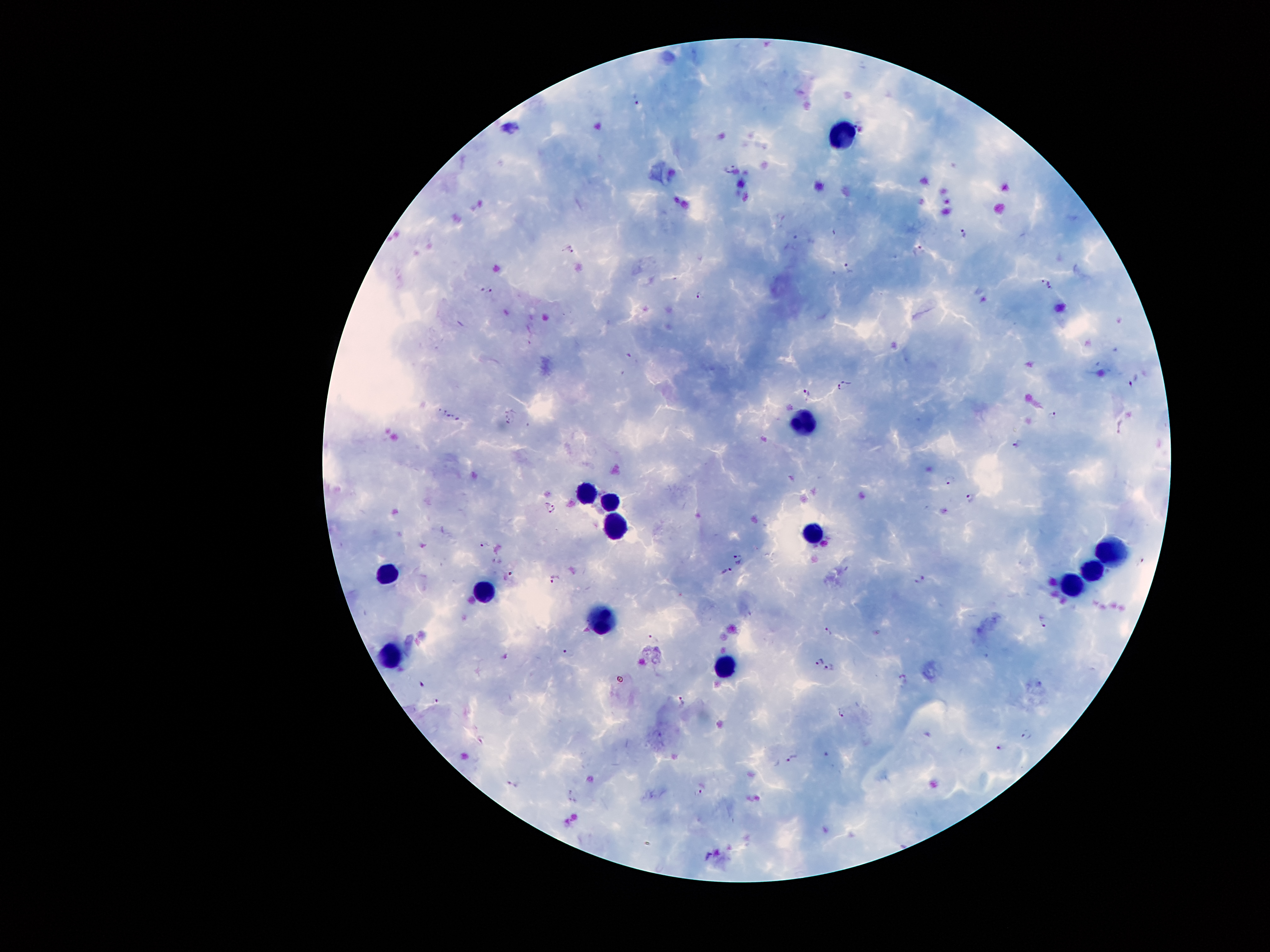

Approximate centers as (x, y) in pixels.
Summary:
  - Leukocyte locations: (842, 132), (801, 417), (584, 487), (606, 500), (611, 525), (811, 535), (1108, 549), (1090, 570), (388, 577), (1071, 582), (482, 589), (602, 617), (392, 652), (724, 665)
  - Plasmodium parasite locations: (637, 99), (730, 167), (964, 234), (568, 247), (917, 251), (848, 268), (1048, 285), (489, 289), (700, 295), (1134, 379), (844, 386), (807, 394), (1053, 414), (449, 415), (459, 418), (1017, 444), (949, 482), (969, 500), (552, 510), (484, 544), (739, 558), (1141, 561), (725, 572), (555, 579), (917, 579), (1046, 621), (827, 633), (654, 639), (569, 652), (504, 658), (818, 660), (829, 665), (902, 679), (421, 684), (683, 700), (840, 712), (1026, 735), (1001, 748), (828, 755), (791, 757), (512, 783), (698, 791), (708, 854)
  - Patient malaria status: positive for Plasmodium falciparum
  - Field of view: single
  - Preparation: thick blood film
  - Capture: smartphone through the microscope eyepiece
  - Stain: Giemsa
  - Image size: 1270×952 pixels
  - Magnification: 100x